Assess this cell for malaria.
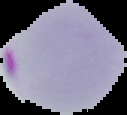

It is parasitized.

The area outside the segmented cell region is set to black. Image is 127×115 pixels. From a thin blood film.